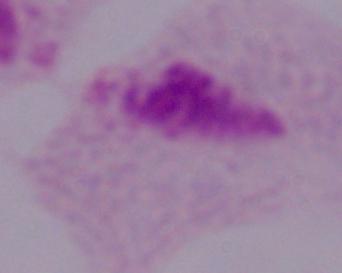

{
  "modality": "micrograph",
  "identification": "trichomonad",
  "magnification": "1000x"
}